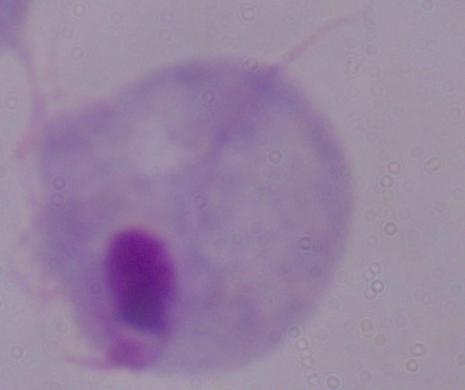 A trichomonad is seen. 1000x magnification. Photomicrograph.